Name the parasite shown.
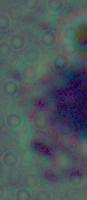

Leishmania.

Micrograph. Captured at 1000x magnification.